Locate the cells, classifying each as a parasitized red blood cell, an uninfected red blood cell, or a white blood cell.
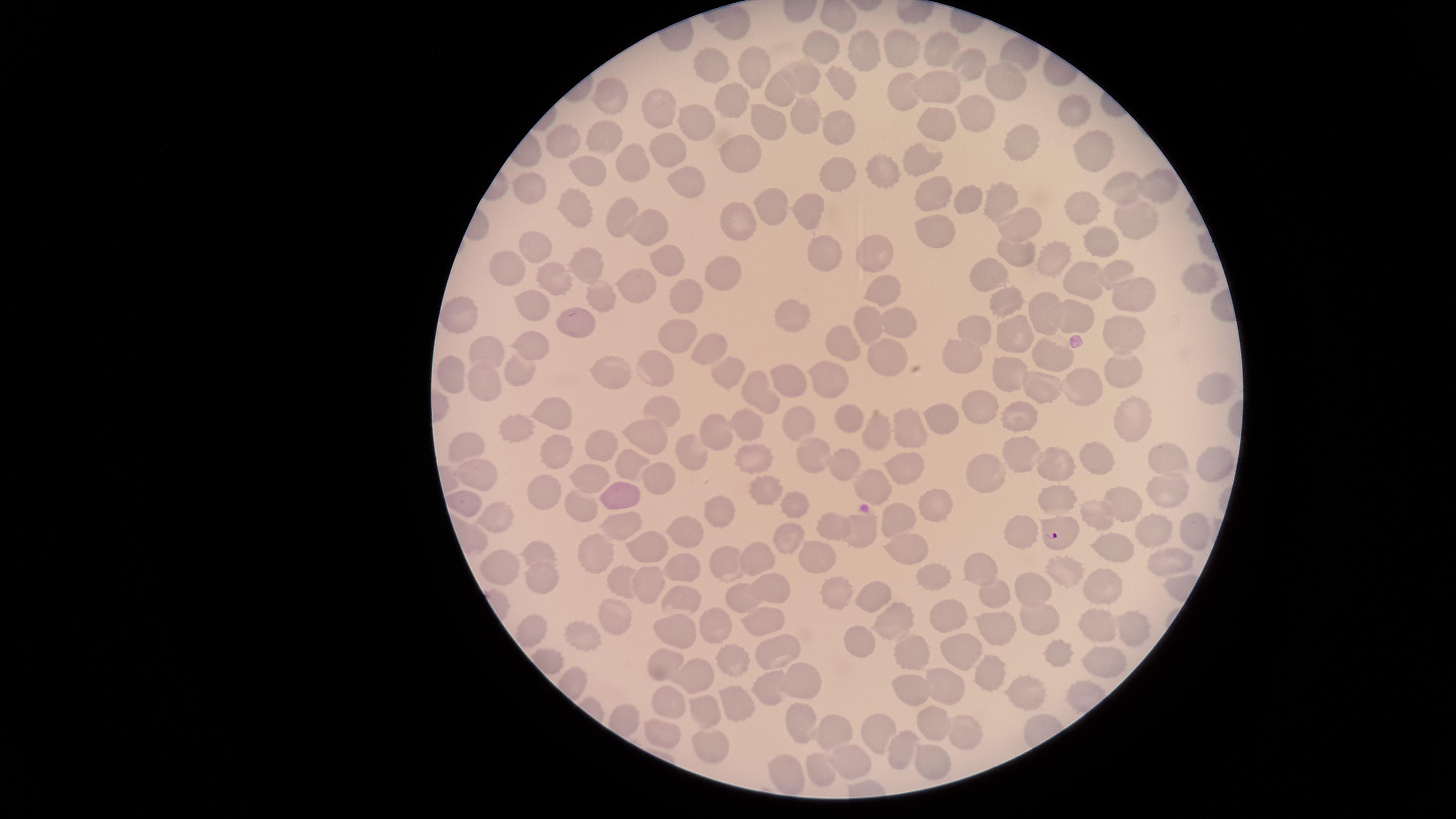
Approximate marker points, in pixels from the top-left corner.
Parasitized red blood cells: (x=1062, y=537).
Uninfected red blood cells: (x=738, y=27), (x=935, y=50), (x=1020, y=51), (x=821, y=52), (x=860, y=52), (x=891, y=55), (x=968, y=67), (x=713, y=69), (x=753, y=72), (x=801, y=77), (x=1002, y=79), (x=841, y=83), (x=943, y=84), (x=778, y=87), (x=901, y=90), (x=610, y=97), (x=733, y=102), (x=654, y=106), (x=1074, y=111), (x=976, y=114), (x=802, y=115), (x=768, y=117), (x=698, y=123), (x=837, y=128), (x=939, y=128), (x=605, y=136), (x=557, y=142), (x=1022, y=142), (x=669, y=149), (x=735, y=157), (x=1091, y=157), (x=918, y=160), (x=634, y=165), (x=882, y=170), (x=585, y=172), (x=835, y=175), (x=690, y=179), (x=1130, y=185), (x=1160, y=185), (x=531, y=188), (x=931, y=189), (x=1003, y=195), (x=969, y=201), (x=768, y=202), (x=578, y=203), (x=807, y=207), (x=1090, y=207), (x=618, y=210), (x=1138, y=220), (x=647, y=223), (x=735, y=227), (x=1014, y=227), (x=934, y=235), (x=1100, y=240), (x=535, y=245), (x=818, y=250), (x=874, y=250), (x=1020, y=251), (x=664, y=256), (x=1058, y=256), (x=582, y=260), (x=1117, y=269), (x=506, y=271), (x=713, y=273), (x=991, y=273), (x=1200, y=276), (x=556, y=277), (x=631, y=281), (x=1080, y=285), (x=881, y=288), (x=598, y=292), (x=1134, y=295), (x=688, y=297), (x=531, y=302), (x=1009, y=302), (x=791, y=310), (x=1080, y=310), (x=1035, y=313), (x=460, y=314), (x=867, y=321), (x=575, y=322), (x=1133, y=329), (x=893, y=332), (x=976, y=334), (x=677, y=337), (x=1018, y=337), (x=843, y=341), (x=704, y=347), (x=486, y=348), (x=529, y=348), (x=884, y=352), (x=1048, y=352), (x=968, y=360), (x=1126, y=362), (x=517, y=364), (x=658, y=364), (x=610, y=368), (x=729, y=369), (x=1014, y=372), (x=448, y=373), (x=796, y=373), (x=835, y=379), (x=481, y=385), (x=1039, y=388), (x=1088, y=388), (x=1210, y=393), (x=752, y=397), (x=975, y=406), (x=552, y=410), (x=660, y=410), (x=1020, y=410), (x=950, y=412), (x=852, y=418), (x=1145, y=419), (x=800, y=423), (x=519, y=426), (x=918, y=427), (x=753, y=428), (x=715, y=432), (x=877, y=432), (x=596, y=437), (x=643, y=437), (x=468, y=444), (x=556, y=446), (x=689, y=449), (x=810, y=456), (x=1018, y=456), (x=903, y=461), (x=839, y=462), (x=1094, y=462), (x=629, y=463), (x=1052, y=463), (x=1171, y=464), (x=753, y=465), (x=479, y=468), (x=986, y=468), (x=1211, y=468), (x=654, y=473), (x=585, y=479), (x=872, y=481), (x=1169, y=493), (x=543, y=494), (x=761, y=495), (x=618, y=497), (x=1061, y=501), (x=1126, y=501), (x=464, y=502), (x=931, y=503), (x=717, y=506), (x=581, y=507), (x=792, y=507), (x=494, y=515), (x=618, y=520), (x=897, y=520), (x=830, y=526), (x=863, y=529), (x=686, y=533), (x=1024, y=535), (x=1156, y=535), (x=787, y=538), (x=1116, y=544), (x=1186, y=545), (x=641, y=547), (x=538, y=548), (x=906, y=550), (x=760, y=556), (x=814, y=558), (x=598, y=560), (x=1160, y=560), (x=502, y=564), (x=720, y=564), (x=687, y=567), (x=979, y=568), (x=1065, y=572), (x=620, y=576), (x=539, y=577), (x=937, y=577), (x=1092, y=582), (x=769, y=584), (x=646, y=585), (x=1032, y=585), (x=872, y=588), (x=838, y=592), (x=685, y=593), (x=743, y=598), (x=997, y=602), (x=943, y=614), (x=888, y=618), (x=1001, y=618), (x=616, y=619), (x=712, y=619), (x=764, y=619), (x=1035, y=620), (x=1130, y=625), (x=1100, y=627), (x=678, y=629), (x=588, y=637), (x=856, y=638), (x=910, y=648), (x=960, y=649), (x=779, y=652), (x=1053, y=656), (x=727, y=660), (x=664, y=661), (x=1103, y=661), (x=990, y=674), (x=696, y=676), (x=1025, y=682), (x=948, y=683), (x=801, y=685), (x=767, y=689), (x=910, y=693), (x=742, y=696), (x=672, y=702), (x=702, y=707), (x=801, y=719), (x=928, y=721), (x=876, y=730), (x=960, y=731), (x=836, y=732), (x=663, y=733), (x=707, y=747), (x=901, y=747), (x=854, y=764), (x=932, y=766), (x=820, y=771), (x=786, y=774).
No white blood cells identified.

Summary:
  - Field of view: single
  - Preparation: thin smear of blood
  - Stain: Giemsa
  - Image size: 1456×819 pixels
  - Species: Plasmodium falciparum
  - Visible region: circular
  - Capture: smartphone photograph through the microscope eyepiece